Assess this cell for malaria.
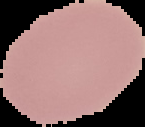
Uninfected.

Summary:
  - Preparation: thin blood film
  - Image size: 145×127 pixels
  - Image type: segmented cell region with the area outside set to black